Assess the morphology of the erythrocytes.
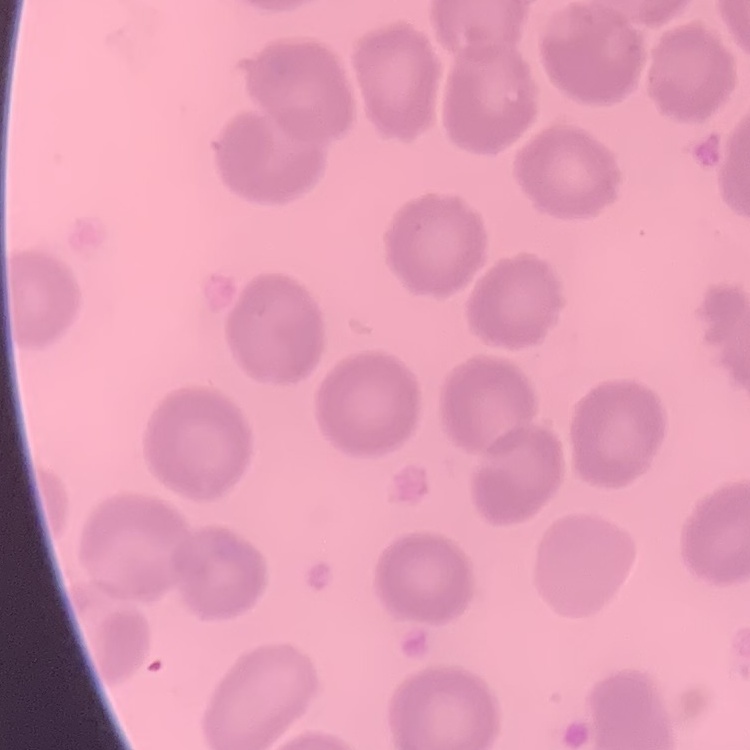

No rouleaux formation.

stain: Field's or Giemsa
image_type: square crop of a larger photomicrograph
preparation: thin blood smear